Classify this cell by malaria status.
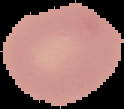
Uninfected.

From a thin blood film. Cell region segmented out of the field of view; the surrounding area is masked to black. Image is 124×109 pixels.